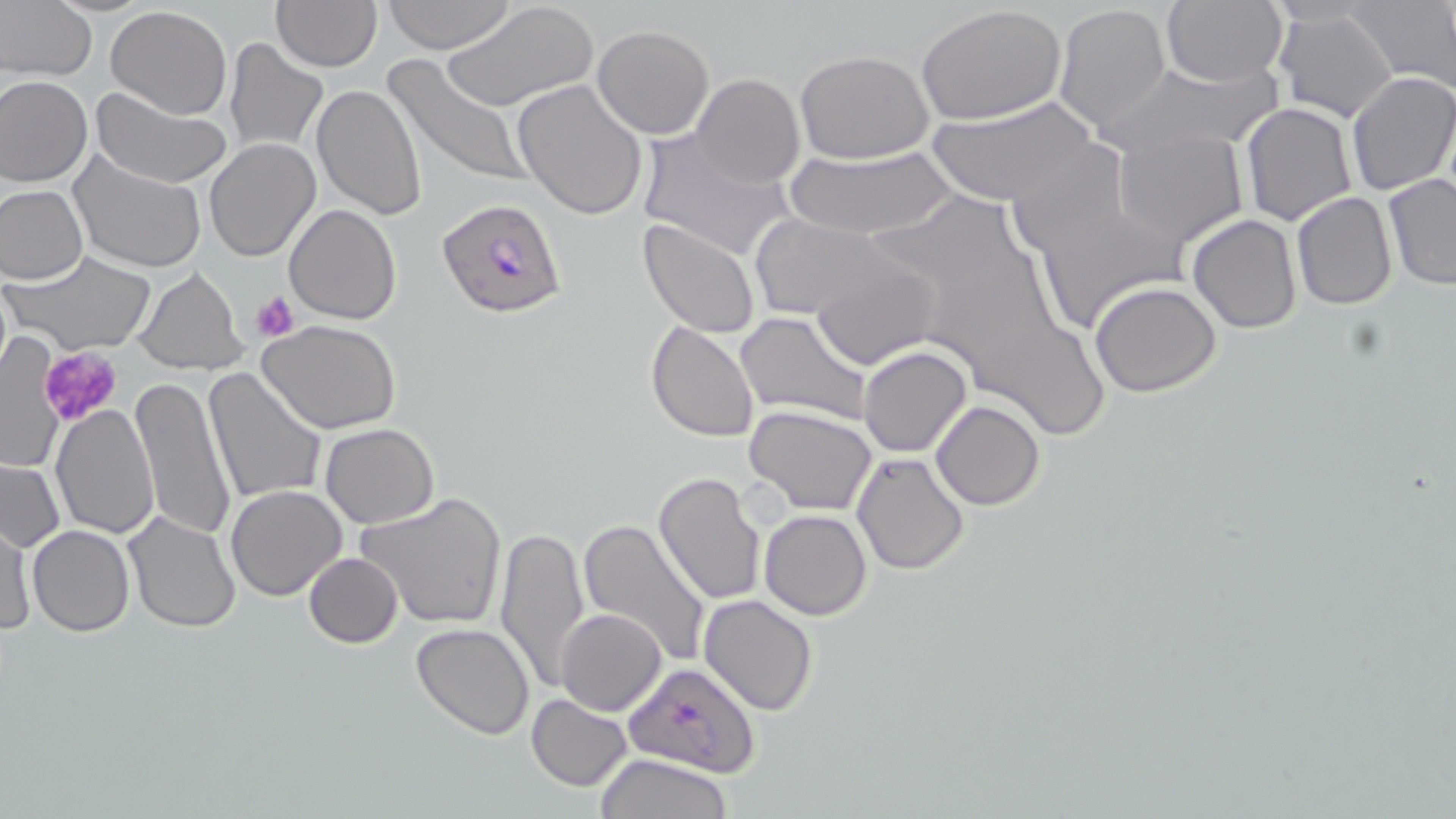 Approximate bounding boxes as (x1, y1, x2, y2) in pixels. Uninfected red blood cell locations: (384, 0, 512, 54), (440, 0, 596, 112), (1159, 0, 1287, 87), (270, 1, 381, 72), (1347, 1, 1456, 90), (0, 4, 97, 81), (917, 4, 1066, 126), (1054, 4, 1170, 131), (104, 5, 233, 120), (1274, 7, 1399, 122), (591, 25, 715, 139), (223, 37, 328, 156), (794, 50, 934, 164), (381, 54, 529, 189), (1100, 62, 1278, 157), (1347, 71, 1456, 196), (691, 73, 804, 189), (0, 74, 93, 187), (513, 78, 649, 220), (312, 81, 428, 220), (89, 86, 231, 189), (1241, 89, 1456, 208), (927, 97, 1102, 208), (1241, 102, 1356, 224), (637, 128, 796, 264), (1112, 128, 1247, 246), (204, 138, 321, 262), (782, 144, 960, 242), (68, 152, 207, 273), (1383, 175, 1456, 291), (1, 184, 87, 285), (1291, 190, 1396, 310), (285, 203, 401, 324), (749, 214, 896, 321), (1188, 214, 1301, 332), (638, 217, 760, 338), (9, 250, 157, 356), (808, 251, 941, 371), (135, 267, 247, 376), (1090, 281, 1222, 397), (735, 310, 872, 425), (259, 318, 404, 435), (647, 320, 759, 441), (1, 336, 66, 477), (860, 346, 970, 457), (203, 368, 326, 506), (128, 375, 237, 541), (931, 400, 1045, 510), (49, 403, 160, 539), (744, 405, 878, 514), (888, 409, 1003, 534), (320, 423, 439, 528), (851, 450, 970, 575), (1, 457, 65, 554), (652, 471, 767, 606), (225, 484, 348, 601), (354, 492, 508, 631), (760, 510, 871, 620), (123, 511, 240, 632), (577, 519, 714, 666), (1, 520, 35, 637), (494, 523, 591, 696), (27, 524, 134, 637), (302, 552, 402, 648), (699, 594, 818, 716), (555, 607, 666, 716), (411, 622, 535, 739), (526, 694, 633, 790), (596, 754, 735, 819). Platelet locations: (252, 290, 301, 341), (37, 344, 123, 430). Plasmodium falciparum-infected red blood cell locations: (435, 196, 568, 320), (623, 661, 763, 776). Slide-level diagnosis: Plasmodium falciparum. Thin blood smear. Optical microscopy. Single field of view. 1000x magnification. Image is 1456×819 pixels. May-Grünwald-Giemsa stain.